Comment on the morphology of the red blood cells.
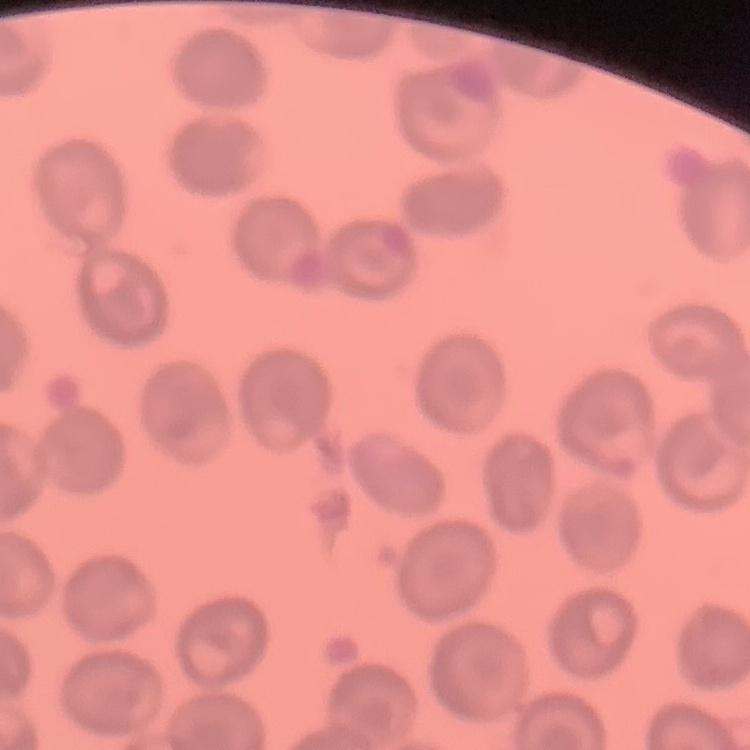
No rouleaux formation.

Square crop of a larger photomicrograph. Thin blood film. Field's or Giemsa stain.